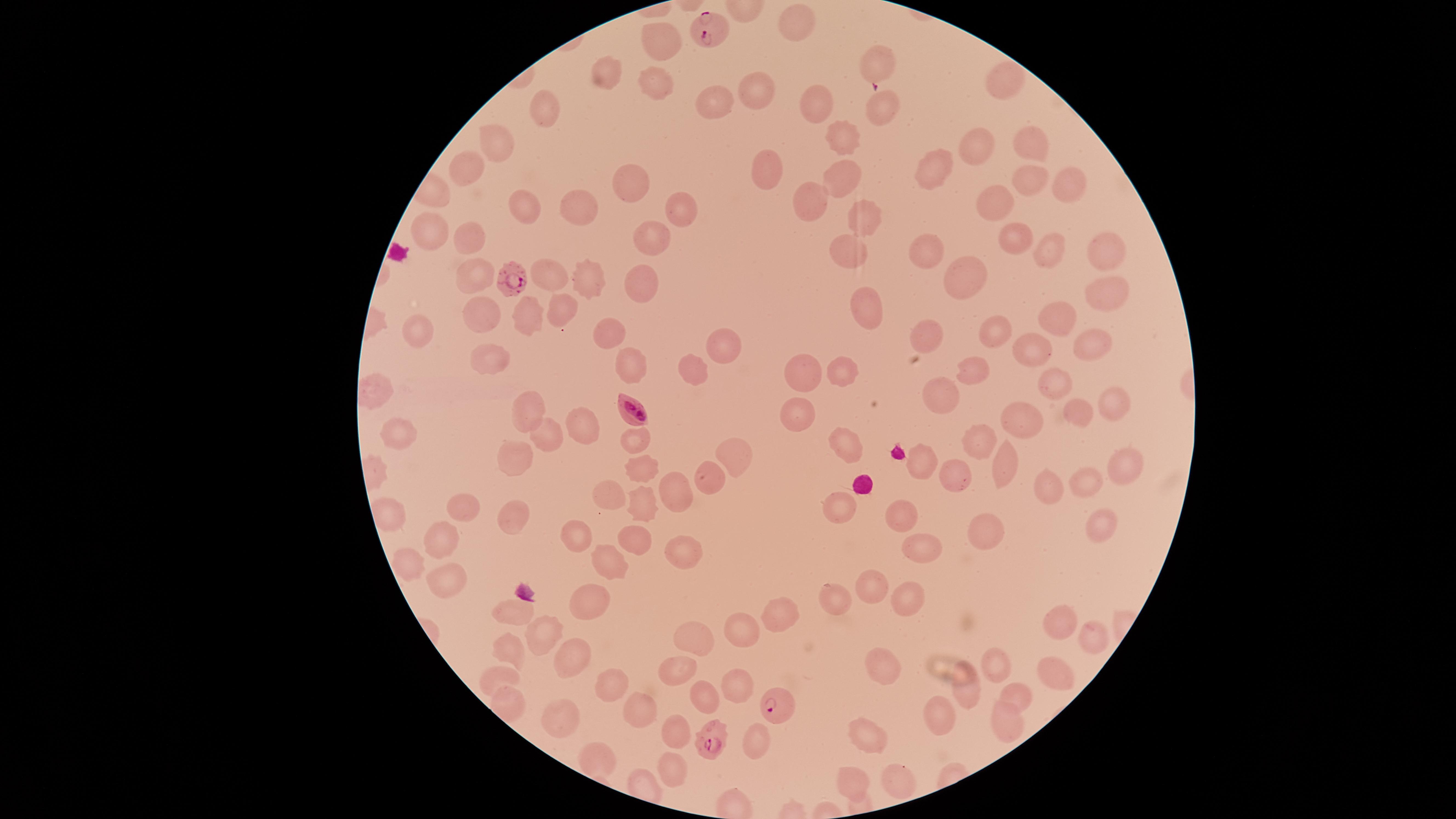
Approximate marker points as (x, y) in pixels. Uninfected RBCs: (798, 22), (663, 42), (877, 64), (608, 73), (654, 80), (1003, 82), (762, 88), (709, 98), (818, 103), (880, 105), (549, 108), (501, 136), (842, 138), (1036, 140), (978, 147), (472, 163), (937, 166), (764, 167), (843, 174), (1026, 177), (625, 184), (1068, 186), (814, 203), (997, 203), (518, 206), (576, 207), (681, 208), (861, 219), (434, 227), (465, 242), (1013, 242), (650, 243), (846, 249), (1058, 250), (1103, 251), (927, 255), (470, 271), (973, 271), (549, 272), (639, 282), (586, 284), (1105, 292), (866, 307), (566, 311), (481, 315), (526, 316), (1055, 319), (426, 329), (992, 331), (608, 333), (925, 338), (1088, 343), (1035, 348), (721, 349), (489, 359), (632, 363), (975, 369), (841, 370), (686, 371), (809, 373), (1053, 378), (940, 388), (1116, 401), (531, 409), (802, 410), (1079, 411), (1024, 417), (581, 422), (405, 435), (549, 436), (636, 437), (982, 438), (846, 444), (515, 455), (736, 456), (923, 462), (641, 463), (1005, 465), (1123, 470), (957, 472), (711, 473), (1085, 482), (1052, 485), (683, 487), (607, 494), (639, 499), (464, 503), (391, 508), (842, 512), (902, 513), (513, 515), (1095, 522), (983, 530), (580, 532), (636, 534), (439, 536), (925, 542), (683, 545), (603, 557), (414, 562), (870, 581), (449, 585), (839, 593), (900, 593), (586, 598), (516, 611), (771, 613), (1063, 616), (741, 631), (547, 633), (1089, 640), (700, 641), (512, 647), (576, 648), (889, 657), (997, 665), (681, 667), (1053, 670), (494, 673), (610, 683), (731, 686), (967, 689), (1013, 694), (703, 697), (508, 702), (640, 706), (947, 714), (556, 715), (1007, 719), (870, 732), (682, 734), (759, 738), (601, 757), (675, 766), (852, 779), (896, 779). Parasitized RBCs: (707, 27), (512, 272), (636, 411), (773, 704), (710, 740). Giemsa stain. Image is 1456×819 pixels. Species: Plasmodium falciparum. Smartphone photograph through the microscope eyepiece. Thin blood film. One field of view of the specimen. Circular visible region. Presence: malaria parasites detected.